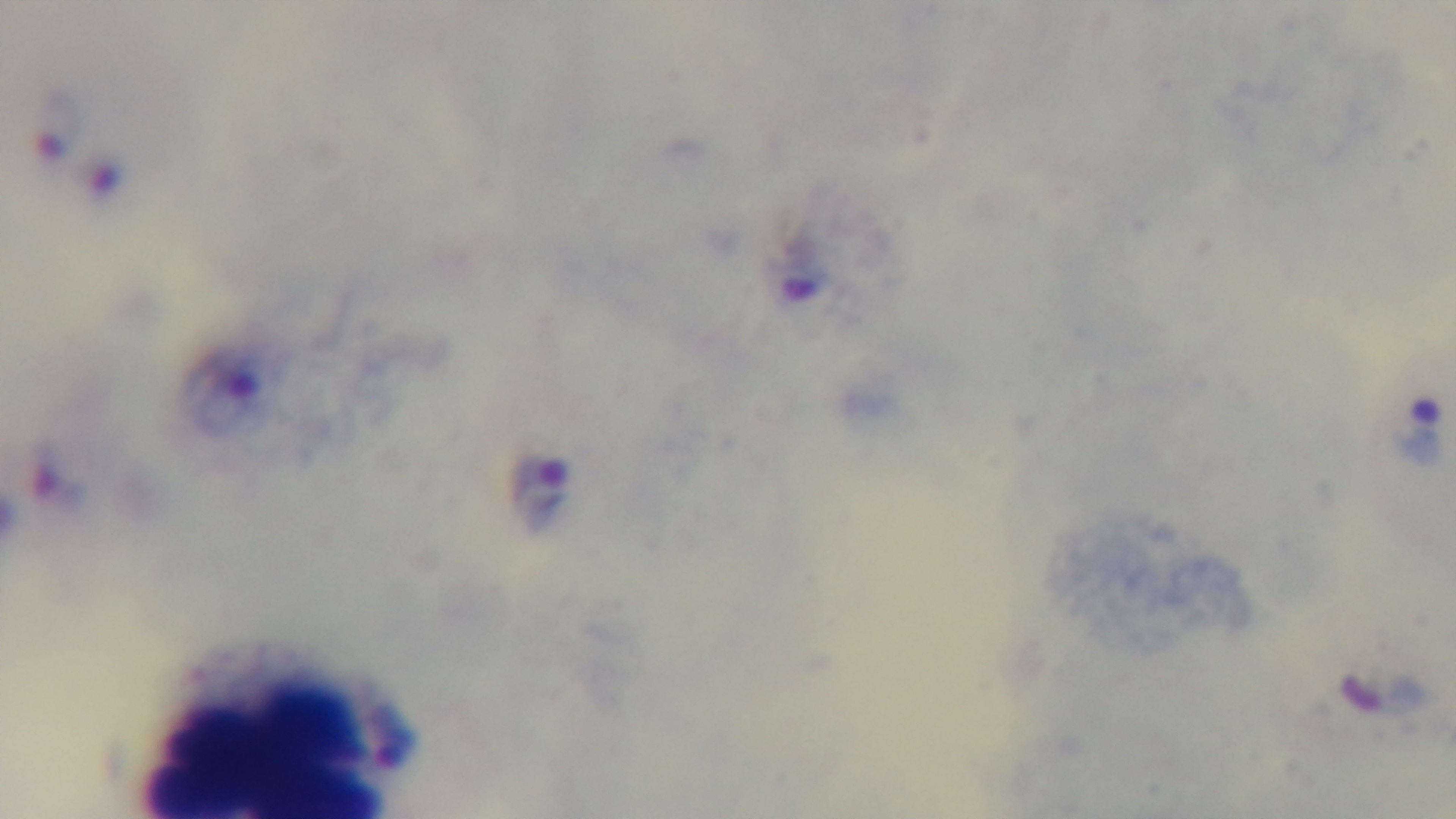

Light microscopy. Oil-immersion objective, 100x. Giemsa stain. Preparation: thick. Captured with a mounted 4K digital camera. Malaria status: infected. One field from the slide.